Outline each Plasmodium vivax-infected red blood cell.
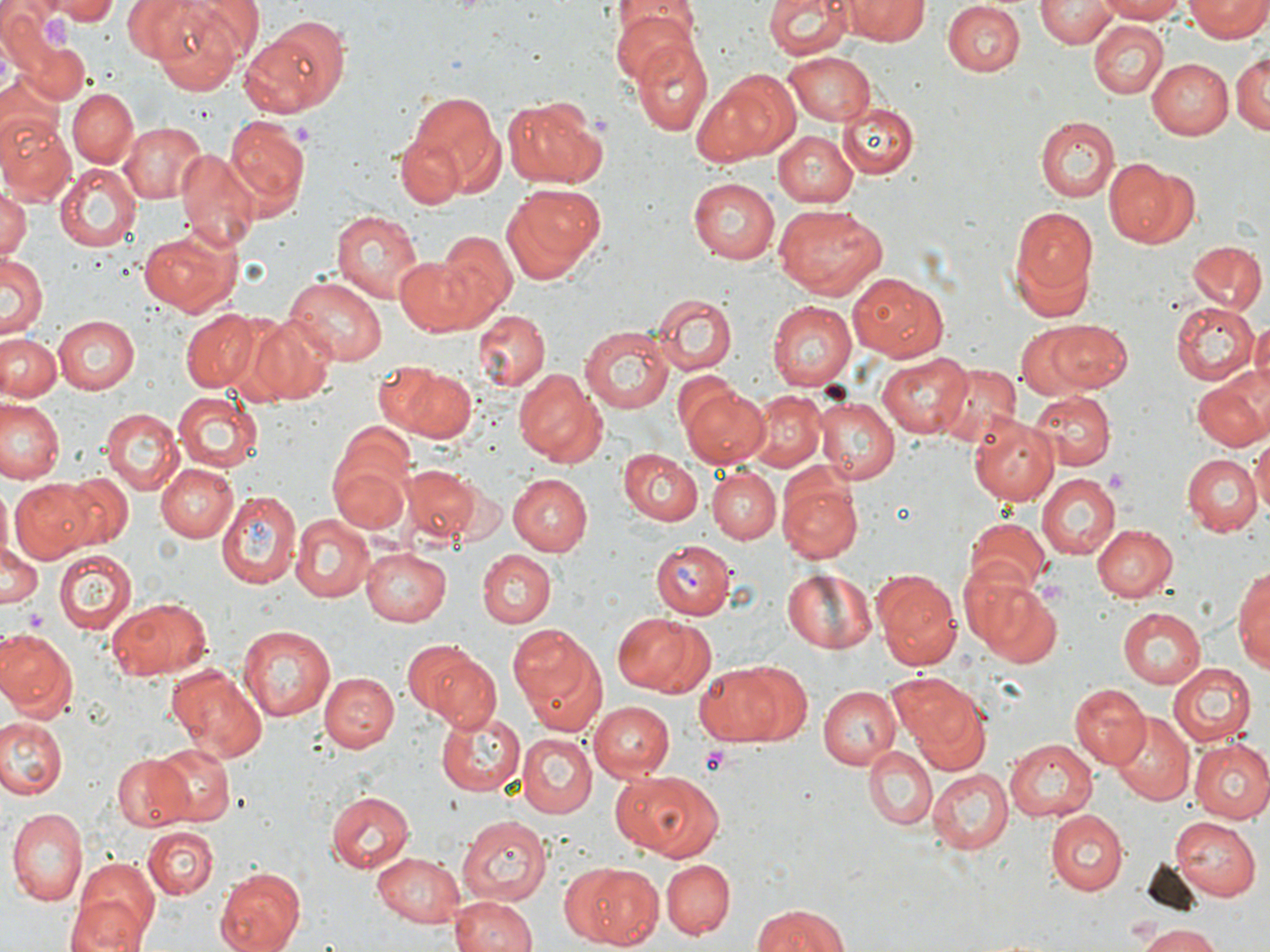
Approximate bounding boxes as (x1,y1)-(x2,y2) corner pairs in pixels.
Plasmodium vivax-infected red blood cells: (650,539)-(734,618).

Summary:
  - Platelet locations: (40,15)-(79,53), (1105,468)-(1127,490), (24,608)-(47,633), (700,746)-(736,779)
  - Uninfected red blood cell locations: (48,0)-(122,23), (764,0)-(851,60), (846,0)-(927,43), (1037,0)-(1116,46), (1094,0)-(1186,22), (122,1)-(196,59), (144,1)-(255,92), (1186,1)-(1268,42), (941,2)-(1024,75), (0,4)-(55,74), (610,6)-(700,83), (251,17)-(352,114), (1091,22)-(1168,100), (630,38)-(715,137), (24,39)-(89,101), (782,50)-(876,123), (1231,50)-(1270,137), (1149,56)-(1234,139), (694,70)-(800,165), (0,74)-(62,156), (67,88)-(138,166), (405,90)-(503,198), (503,96)-(608,191), (839,103)-(919,177), (0,113)-(75,202), (222,114)-(310,217), (1035,116)-(1120,202), (120,121)-(208,204), (397,130)-(472,208), (773,130)-(859,207), (177,147)-(260,251), (1104,157)-(1191,248), (54,164)-(142,254), (687,179)-(780,265), (500,183)-(603,282), (0,186)-(29,264), (773,204)-(887,300), (1011,207)-(1098,298), (329,208)-(424,305), (137,225)-(245,318), (431,231)-(515,327), (1186,242)-(1267,314), (393,255)-(481,336), (2,256)-(46,339), (285,274)-(389,365), (849,274)-(950,361), (648,293)-(737,376), (768,302)-(857,391), (1170,302)-(1258,383), (179,310)-(261,393), (474,311)-(548,390), (244,313)-(339,405), (53,315)-(139,394), (1251,319)-(1270,390), (1045,321)-(1133,391), (1014,324)-(1101,402), (580,326)-(676,413), (1,334)-(64,402), (878,353)-(969,437), (387,362)-(475,442), (929,363)-(1021,452), (513,369)-(604,467), (1192,371)-(1269,452), (678,381)-(769,468), (1028,389)-(1114,469), (171,391)-(263,472), (741,391)-(826,471), (815,396)-(898,484), (1,401)-(66,483), (101,408)-(183,495), (968,415)-(1058,504), (1252,432)-(1270,519), (328,437)-(416,538), (618,448)-(704,524), (1182,454)-(1261,537), (155,462)-(238,541), (404,465)-(482,540), (707,468)-(780,546), (1035,472)-(1120,560), (507,473)-(591,554), (61,475)-(135,546), (777,477)-(861,564), (10,480)-(99,561), (0,488)-(14,557), (216,491)-(301,588), (291,515)-(374,602), (965,518)-(1050,597), (1093,523)-(1177,601), (0,546)-(42,608), (360,546)-(453,624), (477,549)-(555,627), (54,552)-(136,635), (1234,560)-(1270,671), (960,565)-(1062,668), (782,567)-(878,653), (871,568)-(961,670), (106,596)-(214,679), (1117,607)-(1206,688), (612,612)-(710,698), (238,622)-(340,723), (508,623)-(608,735), (0,631)-(77,721), (401,638)-(494,727), (691,659)-(806,745), (1167,662)-(1256,747), (166,665)-(267,763), (318,670)-(398,750), (890,675)-(992,775), (1068,683)-(1149,769), (819,685)-(899,768), (586,701)-(674,781), (434,709)-(525,799), (1109,714)-(1194,803), (0,716)-(66,800), (518,734)-(595,817), (1188,738)-(1270,821), (1004,739)-(1097,821), (150,741)-(235,827), (864,746)-(936,830), (110,751)-(195,831), (608,769)-(723,861), (927,769)-(1014,854), (326,789)-(414,872), (6,809)-(85,905), (1045,811)-(1129,895), (457,815)-(550,903), (1169,816)-(1260,899), (143,826)-(217,899), (370,851)-(467,928), (74,859)-(161,945), (661,859)-(735,937), (564,861)-(665,951), (214,867)-(306,952), (65,895)-(148,952), (450,895)-(537,952), (749,903)-(852,952), (1137,923)-(1225,951)
  - Slide-level diagnosis: Plasmodium vivax
  - Magnification: 1000x
  - Stain: May-Grünwald-Giemsa
  - Image size: 1270×952 pixels
  - Modality: optical microscopy
  - Preparation: thin blood film
  - Field of view: one of a larger specimen